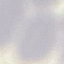 Malaria status: uninfected. Giemsa-stained preparation. Thin blood film. Cell patch, automatically extracted from a larger field of view and resized to 64 × 64 pixels. Photographed with a smartphone camera at the microscope eyepiece.